Give the position of every Plasmodium parasite visible.
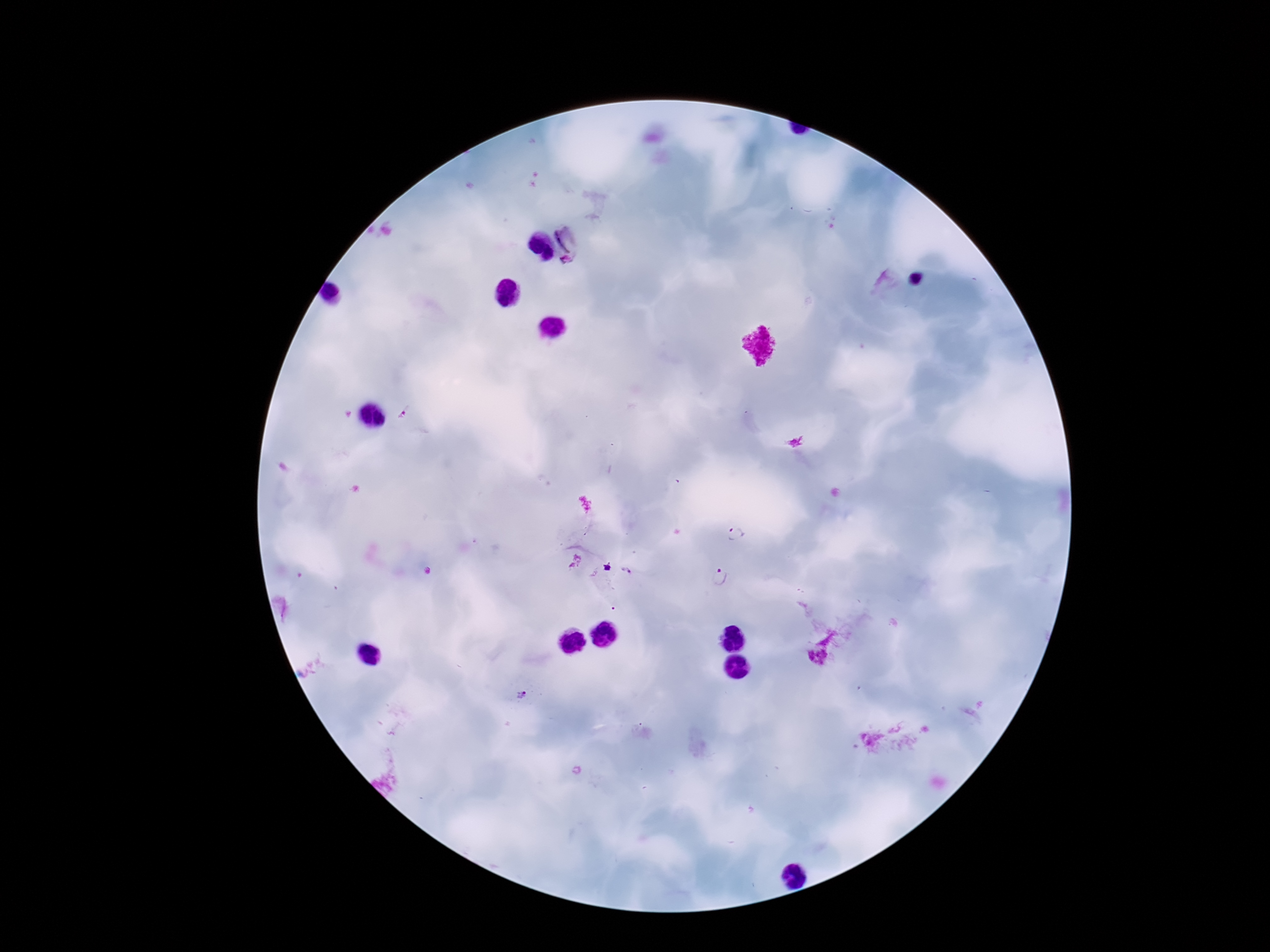

Approximate centers as {x, y} in pixels.
Plasmodium parasites: {572, 233}, {567, 264}, {737, 533}, {575, 561}, {721, 577}, {522, 696}.

Image is 1270×952 pixels. Giemsa-stained preparation. Photographed through the microscope eyepiece with a smartphone camera. 100x magnification. Thick peripheral-blood smear. One field from this slide. Patient malaria status: infected.